Name the parasite shown.
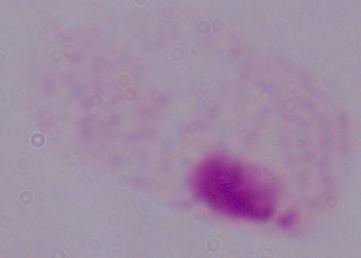

A trichomonad.

magnification = 1000x
modality = micrograph